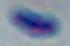 Toxoplasma gondii is seen. Photomicrograph. 1000x magnification.